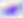
Micrograph. Captured at 400x magnification. Toxoplasma gondii is shown.